Report the malaria status of this cell.
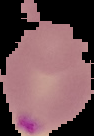

Parasitized.

{
  "image_size": "94×136 pixels",
  "image_type": "cell region segmented out of the field of view; surrounding area masked to black",
  "preparation": "thin blood smear"
}